State which cell type is depicted.
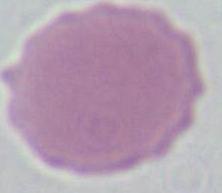
This is an erythrocyte.

Micrograph. 1000x magnification.